State which parasite is depicted.
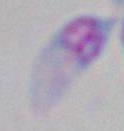
Toxoplasma gondii.

magnification: 1000x
modality: micrograph